Outline each blood parasite and name the species.
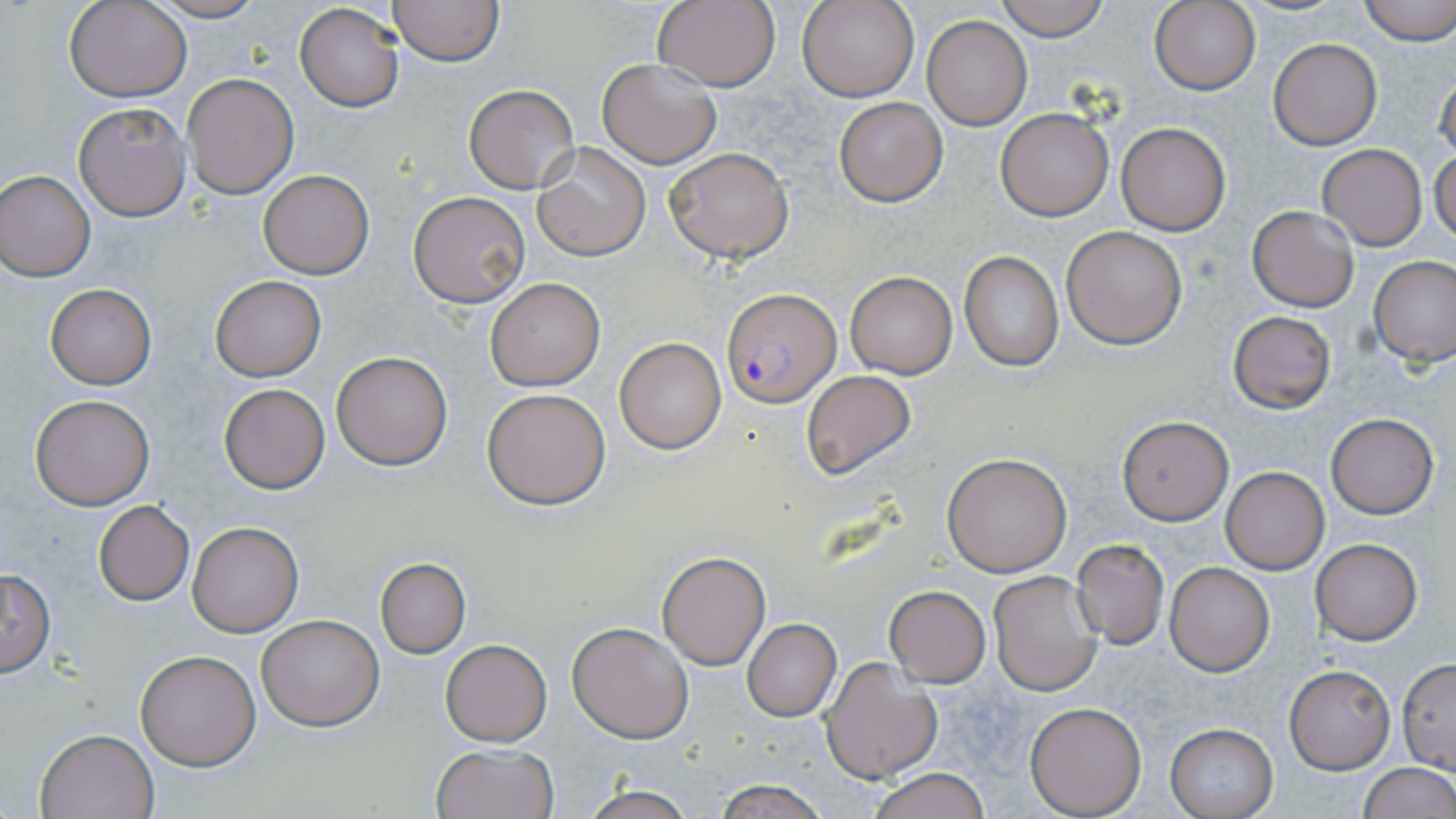

Approximate bounding boxes as (x1,y1)-(x2,y2) corner pairs in pixels.
Plasmodium falciparum-infected red blood cells: (722,288)-(841,406).
No Plasmodium ovale, Plasmodium malariae, Plasmodium vivax, Babesia divergens, or Trypanosoma brucei observed.

Summary:
  - Uninfected red blood cell locations: (66,0)-(191,102), (140,0)-(274,23), (651,0)-(780,91), (993,0)-(1109,40), (1356,0)-(1456,44), (389,1)-(504,66), (797,1)-(919,103), (1151,1)-(1261,94), (294,3)-(404,114), (921,15)-(1032,129), (1267,38)-(1381,150), (597,58)-(723,168), (1434,67)-(1455,166), (183,74)-(298,198), (464,85)-(579,193), (832,97)-(948,206), (74,103)-(190,220), (996,107)-(1113,221), (1114,121)-(1231,236), (532,142)-(651,261), (1317,144)-(1426,249), (663,146)-(793,263), (1431,146)-(1456,247), (259,170)-(374,278), (0,171)-(96,280), (408,190)-(531,308), (1247,206)-(1359,312), (1062,225)-(1188,349), (960,252)-(1063,372), (1368,255)-(1456,365), (843,270)-(958,378), (210,276)-(325,381), (485,278)-(606,390), (46,284)-(156,390), (1227,310)-(1336,413), (613,337)-(726,453), (332,351)-(454,470), (801,370)-(916,479), (219,384)-(330,494), (482,387)-(611,510), (30,394)-(154,509), (1326,414)-(1437,518), (1117,416)-(1233,525), (941,453)-(1073,576), (1220,467)-(1330,573), (93,500)-(195,604), (187,520)-(304,637), (1309,539)-(1422,644), (1070,540)-(1169,648), (657,551)-(770,669), (376,558)-(470,657), (1165,563)-(1275,675), (1,568)-(56,676), (988,570)-(1102,695), (884,585)-(990,686), (257,614)-(384,730), (742,619)-(841,720), (567,621)-(693,742), (441,640)-(552,746), (135,648)-(260,770), (820,658)-(943,784), (1397,659)-(1455,772), (1284,663)-(1396,774), (921,670)-(1039,779), (1025,700)-(1148,817), (1164,723)-(1278,818), (36,729)-(158,818), (432,744)-(559,819), (1357,763)-(1456,819), (867,767)-(990,819), (713,779)-(832,818), (580,785)-(699,819)
  - Slide-level diagnosis: Plasmodium falciparum
  - Preparation: thin blood film
  - Stain: May-Grünwald-Giemsa
  - Magnification: 1000x
  - Modality: light microscopy
  - Image size: 1456×819 pixels
  - Field of view: one of a larger specimen